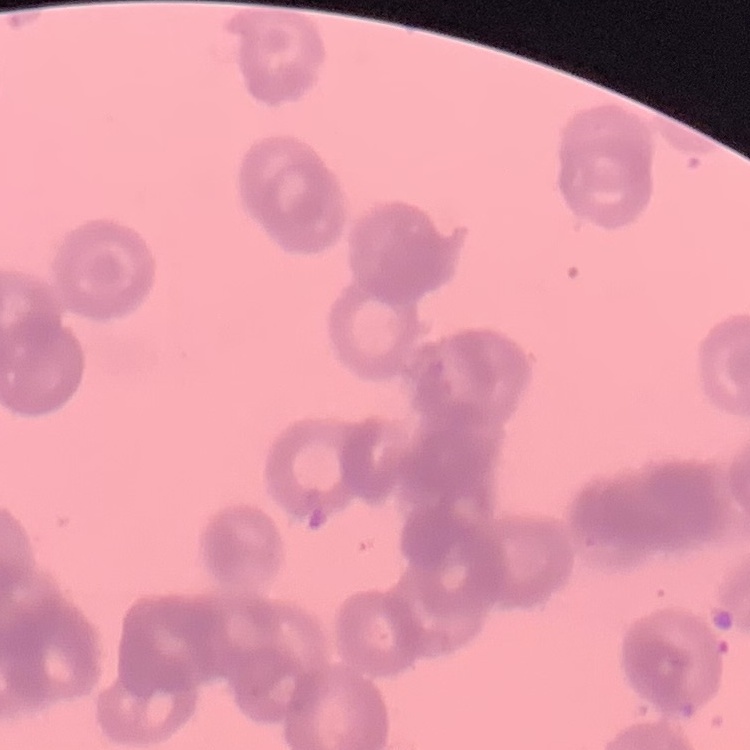
erythrocyte_morphology: rouleaux formation
preparation: thin blood film
stain: Field's or Giemsa
image_type: square crop of a larger photomicrograph